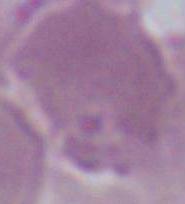
Summary:
  - Modality: micrograph
  - Identification: red blood cell
  - Magnification: 1000x